Locate and identify every blood parasite.
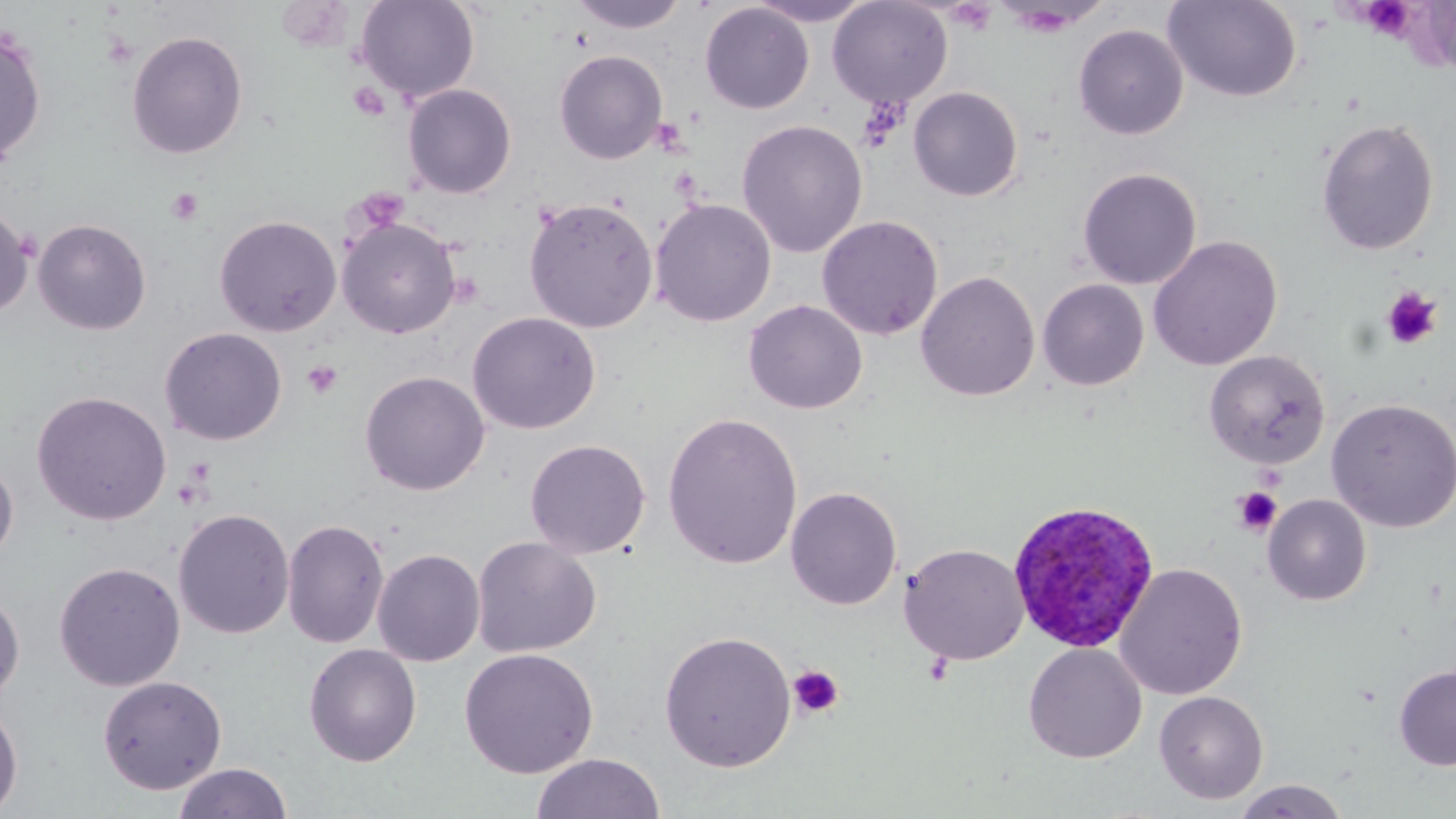

Approximate bounding boxes as (x1, y1, x2, y2) in pixels.
Plasmodium ovale-infected red blood cells: (1006, 499, 1160, 652).
No Plasmodium falciparum, Plasmodium malariae, Plasmodium vivax, Babesia divergens, or Trypanosoma brucei observed.

Summary:
  - Uninfected red blood cell locations: (355, 0, 480, 102), (568, 0, 691, 34), (746, 0, 875, 26), (827, 0, 953, 108), (1164, 0, 1301, 102), (699, 3, 814, 114), (1073, 23, 1188, 140), (0, 27, 47, 167), (126, 29, 248, 160), (553, 49, 668, 164), (402, 83, 517, 199), (908, 85, 1024, 202), (1316, 118, 1439, 255), (736, 119, 868, 258), (1077, 167, 1202, 289), (523, 196, 658, 333), (650, 198, 776, 327), (0, 208, 36, 316), (214, 214, 342, 337), (816, 214, 944, 341), (337, 217, 461, 339), (33, 218, 152, 335), (1147, 235, 1283, 371), (916, 270, 1040, 402), (1037, 278, 1149, 390), (743, 299, 868, 414), (466, 311, 601, 434), (159, 327, 288, 446), (1204, 350, 1330, 469), (359, 370, 491, 496), (32, 390, 172, 525), (1326, 398, 1456, 533), (662, 411, 803, 570), (524, 438, 651, 559), (0, 457, 18, 564), (785, 486, 902, 611), (1262, 494, 1371, 606), (173, 508, 295, 639), (282, 518, 389, 649), (471, 536, 602, 658), (899, 542, 1029, 665), (372, 548, 486, 667), (53, 561, 186, 692), (1114, 562, 1248, 700), (0, 589, 25, 704), (659, 630, 797, 772), (302, 643, 422, 766), (1024, 643, 1147, 764), (459, 647, 599, 779), (1394, 664, 1456, 771), (97, 675, 227, 795), (1154, 690, 1269, 804), (0, 698, 23, 816), (531, 752, 666, 819), (172, 762, 293, 819), (1232, 779, 1351, 818)
  - Platelet locations: (1367, 2, 1413, 45), (101, 30, 139, 69), (348, 82, 390, 121), (857, 96, 910, 150), (650, 117, 688, 155), (165, 187, 204, 226), (1381, 286, 1442, 350), (301, 360, 343, 400), (1234, 487, 1282, 535), (787, 664, 844, 720)
  - Slide-level diagnosis: Plasmodium ovale
  - Field of view: one of a larger specimen
  - Modality: optical microscopy
  - Image size: 1456×819 pixels
  - Magnification: 1000x
  - Preparation: thin blood smear
  - Stain: May-Grünwald-Giemsa